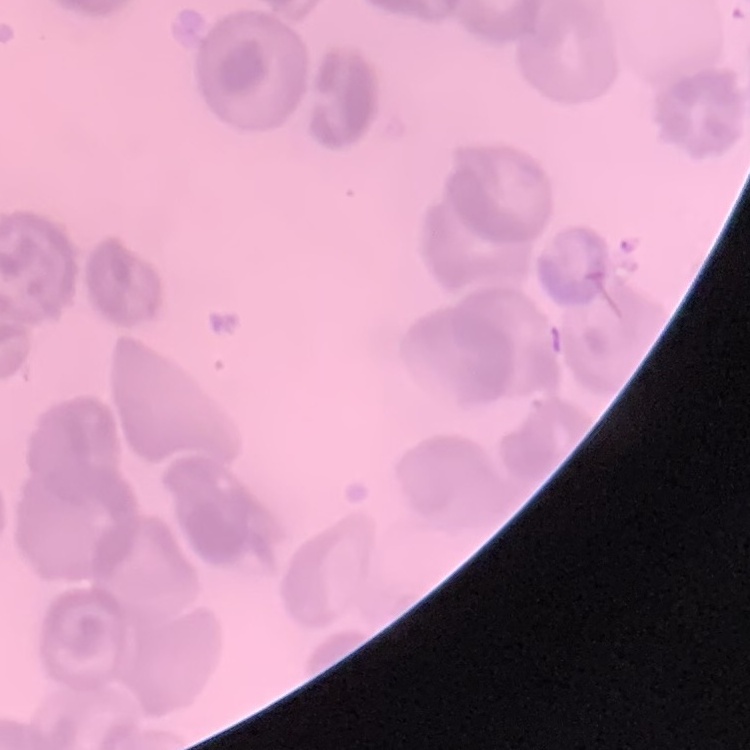

Summary:
  - Erythrocyte morphology: no rouleaux formation
  - Image type: one tile cut from a larger photomicrograph
  - Stain: Field's or Giemsa
  - Preparation: thin blood film